State the blood parasite species.
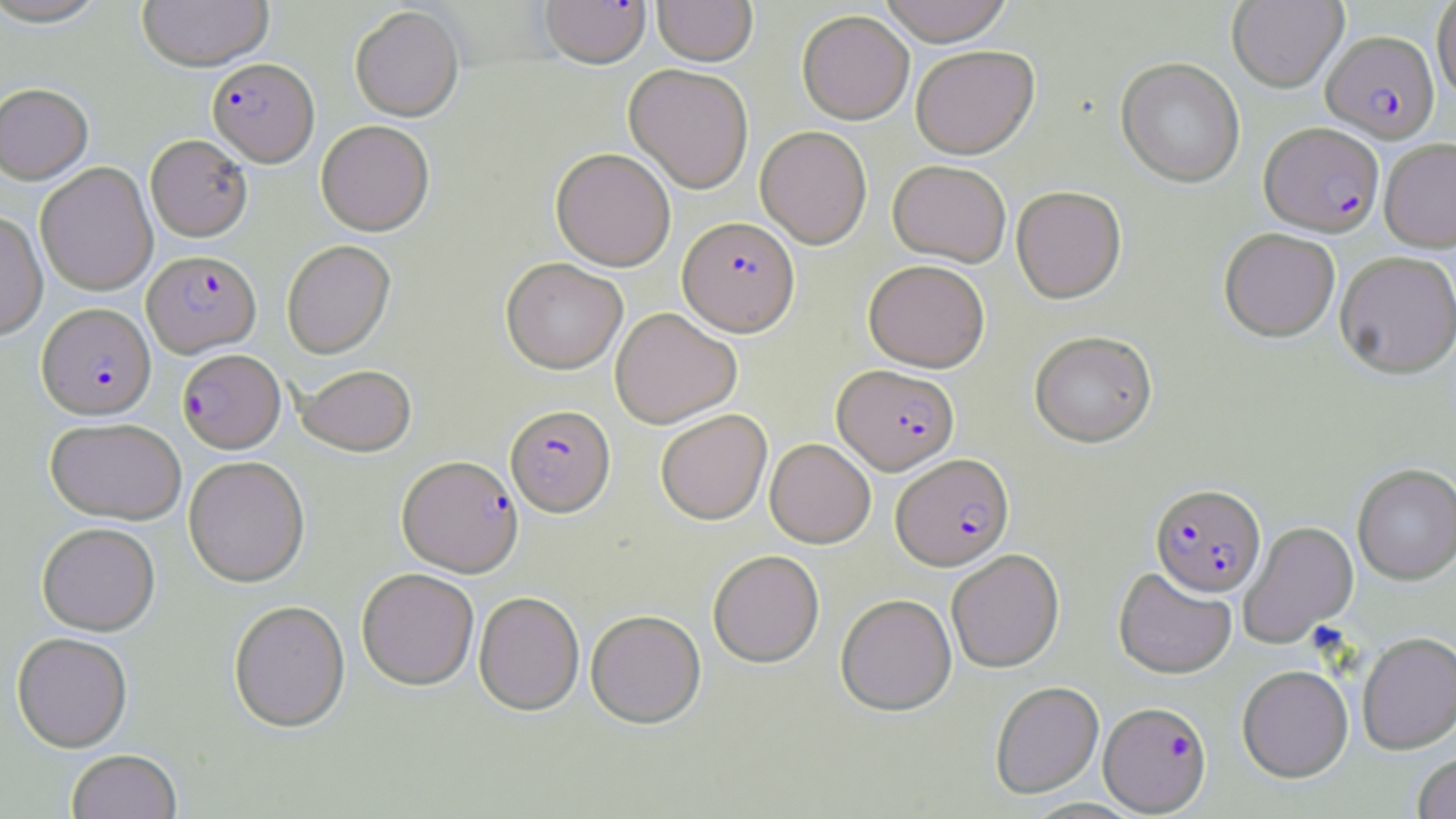
Plasmodium falciparum.

preparation = thin blood smear
uninfected red blood cell locations = approximate bounding boxes as (x1, y1, x2, y2) in pixels: (0, 0, 111, 27), (137, 0, 273, 71), (652, 0, 757, 66), (877, 0, 1015, 46), (1227, 0, 1348, 92), (1431, 0, 1456, 102), (350, 6, 464, 122), (797, 11, 914, 124), (911, 46, 1039, 160), (1116, 58, 1245, 188), (624, 63, 754, 193), (0, 82, 93, 184), (316, 120, 434, 236), (755, 126, 872, 249), (145, 134, 252, 241), (1379, 138, 1456, 252), (550, 147, 676, 271), (888, 160, 1011, 267), (35, 162, 158, 296), (1011, 186, 1127, 304), (0, 211, 48, 339), (1219, 228, 1341, 342), (281, 240, 395, 359), (1334, 250, 1456, 379), (501, 258, 628, 374), (863, 259, 990, 372), (610, 307, 742, 428), (1029, 330, 1158, 447), (296, 364, 417, 456), (656, 409, 772, 525), (45, 417, 186, 524), (765, 438, 876, 548), (183, 455, 310, 587), (1352, 463, 1456, 585), (1238, 521, 1358, 648), (37, 522, 160, 635), (947, 548, 1065, 672), (708, 550, 824, 668), (357, 567, 479, 689), (1113, 567, 1237, 679), (474, 591, 584, 715), (836, 593, 957, 715), (228, 600, 350, 732), (586, 609, 706, 729), (12, 632, 133, 751), (1357, 632, 1456, 754), (1237, 664, 1353, 782), (990, 681, 1104, 799), (66, 748, 183, 819), (1413, 752, 1456, 818)
stain = May-Grünwald-Giemsa
image size = 1456×819 pixels
magnification = 1000x
modality = light microscopy
field of view = one of a larger specimen
Plasmodium falciparum-infected red blood cell locations = approximate bounding boxes as (x1, y1, x2, y2) in pixels: (539, 0, 651, 68), (1322, 30, 1439, 143), (207, 57, 319, 166), (1259, 122, 1384, 236), (678, 216, 800, 336), (142, 250, 261, 357), (37, 302, 155, 419), (177, 349, 286, 453), (833, 365, 960, 475), (505, 404, 615, 517), (891, 453, 1014, 570), (398, 455, 523, 576), (1151, 483, 1267, 597), (1099, 701, 1212, 815)